Report the malaria status of this cell.
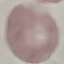

It is uninfected.

Thin blood smear. Giemsa stain. Acquired by smartphone through the microscope eyepiece. Automatically extracted cell patch, resized to 64 × 64 pixels.